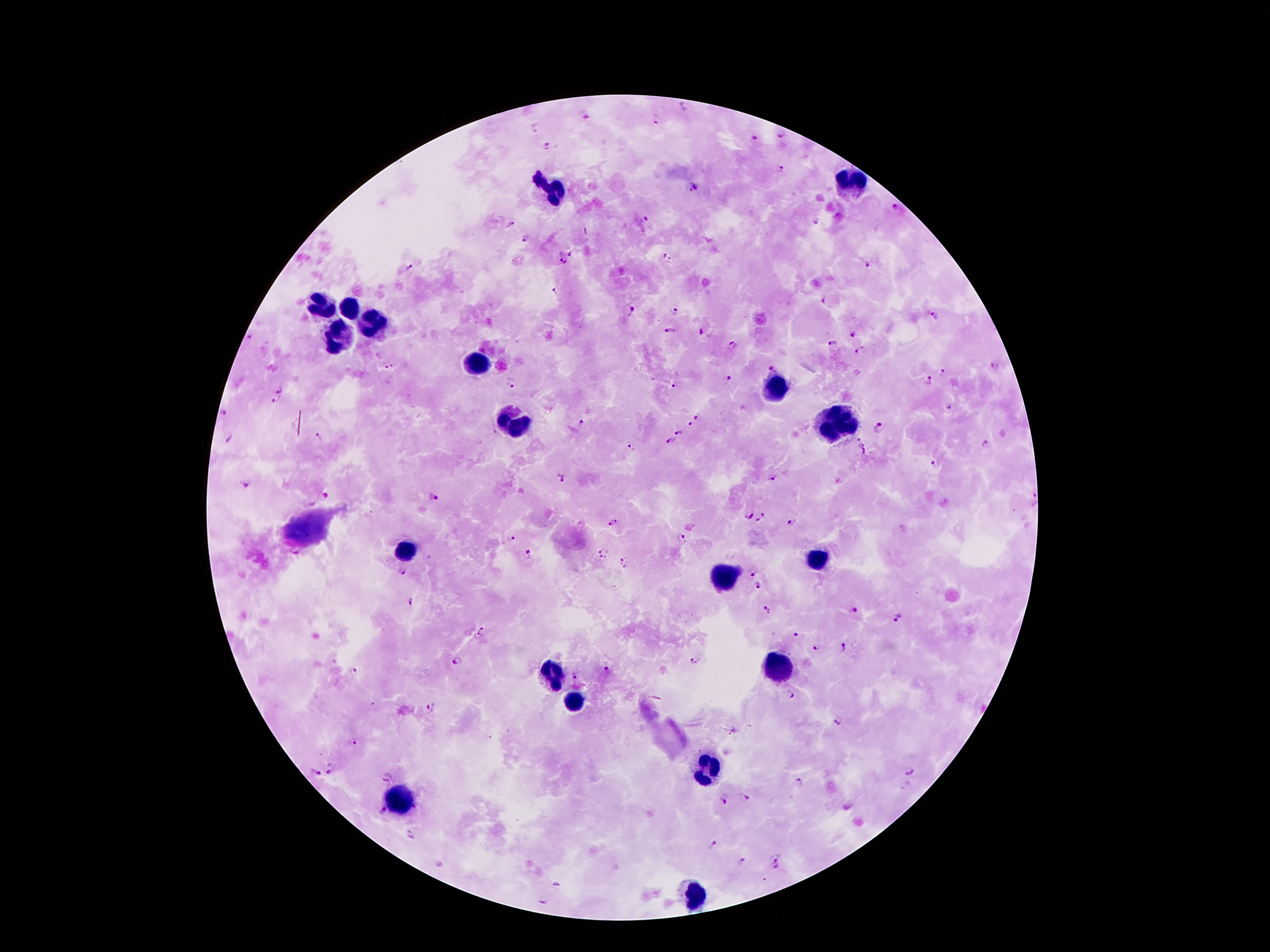

Approximate centers as {x, y} in pixels.
Summary:
  - Leukocyte locations: {851, 180}, {553, 191}, {322, 304}, {347, 307}, {371, 324}, {341, 340}, {478, 364}, {776, 388}, {517, 420}, {838, 427}, {409, 551}, {816, 556}, {723, 574}, {777, 669}, {548, 677}, {574, 702}, {706, 770}, {401, 797}, {695, 893}
  - Plasmodium parasite locations: {683, 109}, {583, 114}, {657, 119}, {535, 127}, {780, 134}, {754, 138}, {548, 146}, {780, 168}, {694, 187}, {896, 210}, {645, 218}, {512, 223}, {818, 223}, {525, 238}, {571, 252}, {668, 258}, {562, 262}, {865, 265}, {410, 266}, {558, 291}, {826, 300}, {632, 311}, {675, 313}, {935, 315}, {668, 330}, {700, 331}, {853, 334}, {250, 337}, {833, 344}, {732, 345}, {861, 349}, {389, 366}, {994, 366}, {774, 367}, {941, 372}, {730, 377}, {928, 380}, {513, 383}, {676, 387}, {281, 389}, {274, 401}, {950, 407}, {224, 414}, {698, 416}, {580, 423}, {690, 423}, {878, 426}, {678, 433}, {320, 436}, {229, 437}, {672, 441}, {985, 443}, {863, 445}, {631, 446}, {937, 462}, {771, 477}, {563, 478}, {246, 483}, {327, 497}, {1031, 498}, {434, 499}, {749, 513}, {764, 513}, {758, 521}, {791, 521}, {614, 522}, {680, 536}, {511, 539}, {601, 548}, {531, 556}, {603, 558}, {623, 558}, {621, 568}, {754, 569}, {402, 570}, {758, 587}, {409, 602}, {855, 609}, {766, 611}, {897, 615}, {482, 632}, {796, 637}, {817, 646}, {842, 648}, {459, 661}, {695, 662}, {353, 669}, {608, 669}, {574, 676}, {789, 696}, {433, 708}, {838, 720}, {355, 742}, {330, 767}, {909, 770}, {316, 772}, {387, 778}, {799, 781}, {725, 798}, {744, 798}, {419, 807}, {380, 814}, {410, 834}, {713, 844}, {777, 856}, {741, 861}, {775, 870}, {557, 885}, {544, 900}
  - Patient malaria status: infected with Plasmodium falciparum
  - Field of view: single
  - Image size: 1270×952 pixels
  - Capture: smartphone through the microscope eyepiece
  - Stain: Giemsa
  - Preparation: thick blood smear
  - Magnification: 100x